Classify this cell by malaria status.
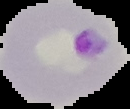

It is parasitized.

preparation = thin blood smear
image type = segmented cell region on a black background
image size = 130×109 pixels